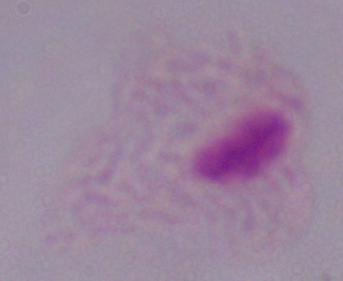

Summary:
  - Magnification: 1000x
  - Modality: micrograph
  - Identification: trichomonad